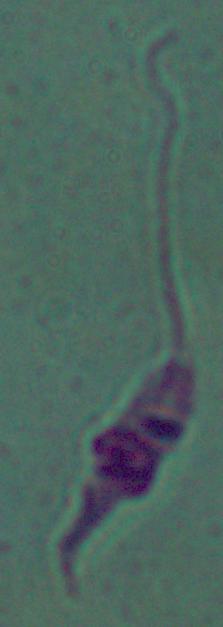
magnification = 1000x
identification = Leishmania
modality = photomicrograph